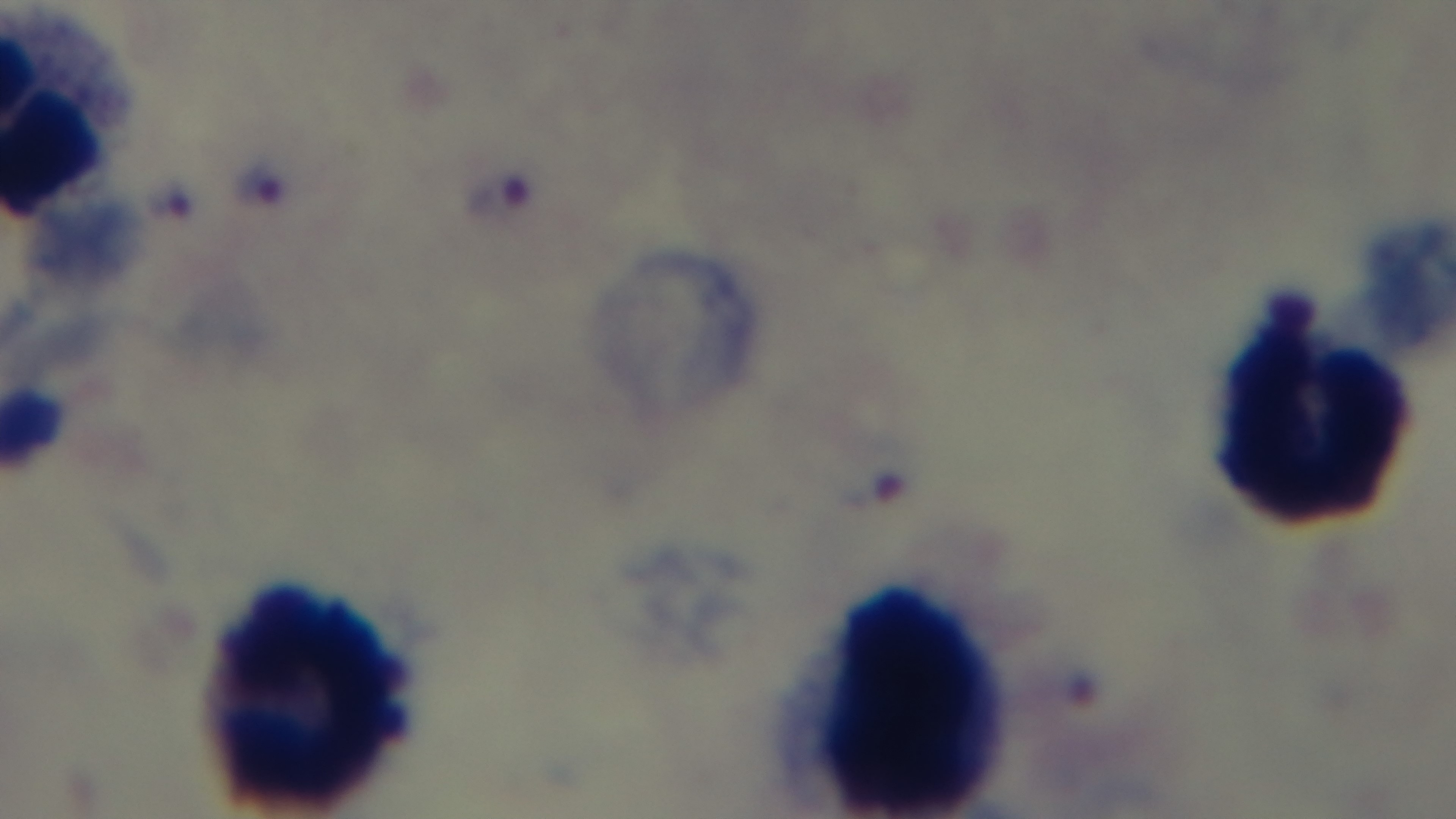

preparation = thick blood film
capture = mounted 4K digital camera
objective = 100x oil immersion
field of view = single
modality = light microscopy
malaria status = positive
stain = Giemsa